Classify this cell by malaria status.
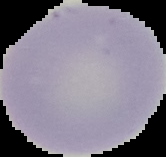
It is uninfected.

Summary:
  - Image type: cell region segmented out of the field of view; surrounding area masked to black
  - Image size: 166×157 pixels
  - Preparation: thin blood film